Outline each blood parasite and name the species.
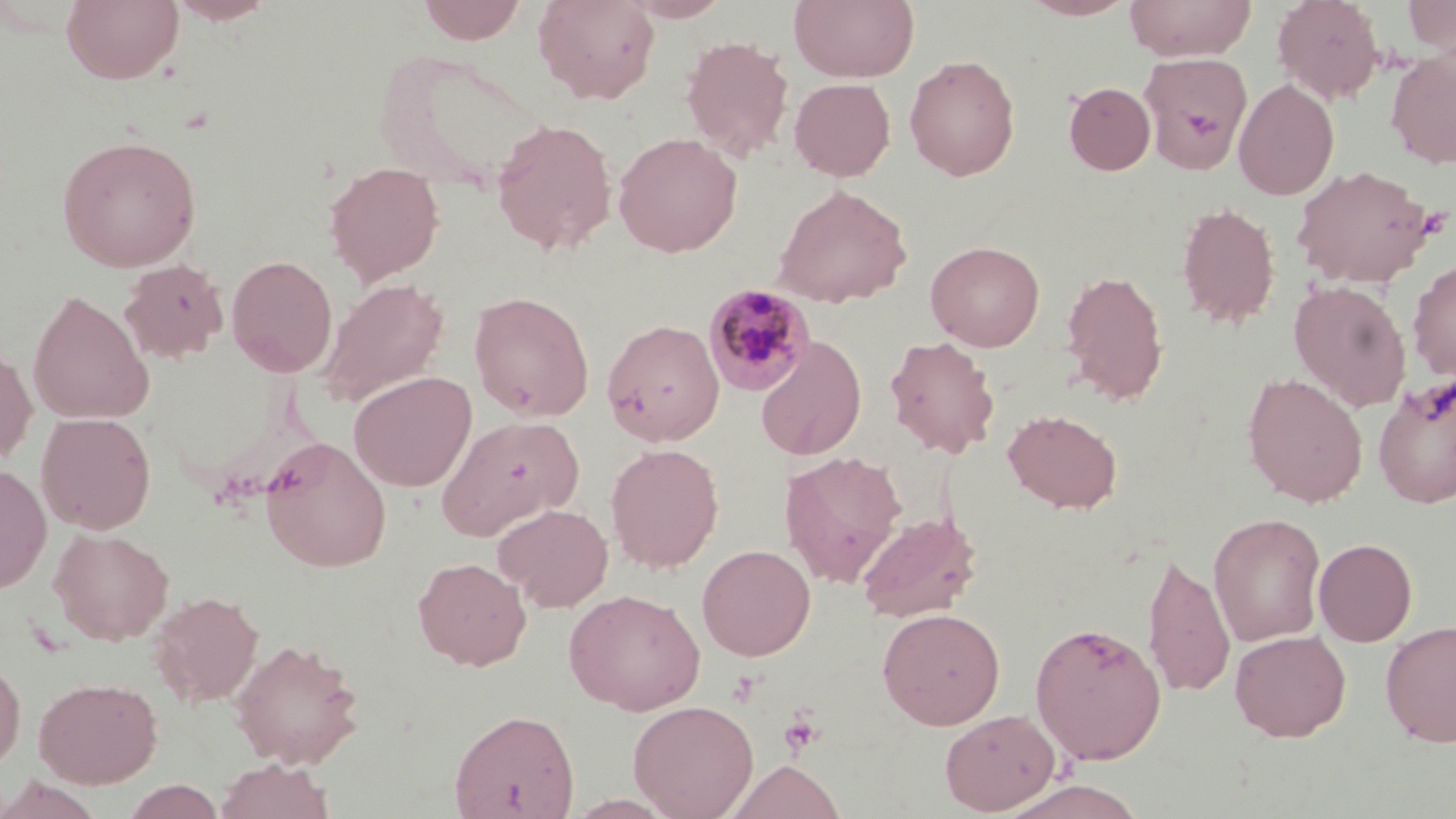

Approximate bounding boxes as [x1, y1, x2, y2] in pixels.
Plasmodium malariae-infected red blood cells: [703, 283, 816, 397].
No Plasmodium falciparum, Plasmodium ovale, Plasmodium vivax, Babesia divergens, or Trypanosoma brucei observed.

Summary:
  - Platelet locations: [777, 709, 825, 759]
  - Uninfected red blood cell locations: [61, 0, 184, 85], [165, 0, 279, 25], [416, 0, 528, 44], [532, 0, 661, 104], [621, 0, 733, 22], [789, 0, 919, 83], [1020, 0, 1138, 20], [1123, 0, 1257, 62], [1272, 0, 1385, 104], [1403, 0, 1455, 58], [680, 35, 794, 162], [375, 50, 551, 196], [1386, 50, 1456, 169], [1138, 52, 1252, 172], [903, 54, 1020, 180], [789, 78, 896, 181], [1233, 79, 1339, 200], [1063, 81, 1155, 175], [491, 118, 618, 255], [613, 132, 743, 257], [56, 135, 202, 272], [324, 161, 444, 285], [1292, 164, 1437, 288], [772, 184, 912, 308], [1176, 202, 1280, 329], [925, 239, 1045, 351], [226, 255, 338, 377], [1407, 258, 1456, 381], [119, 259, 229, 364], [1060, 268, 1169, 404], [319, 278, 449, 407], [1290, 280, 1411, 411], [27, 290, 154, 426], [468, 291, 594, 421], [601, 318, 725, 446], [755, 335, 867, 461], [884, 335, 1000, 459], [0, 342, 38, 468], [348, 370, 477, 491], [1243, 373, 1367, 507], [1372, 374, 1456, 509], [1003, 409, 1122, 513], [36, 412, 156, 534], [437, 414, 585, 540], [259, 436, 393, 572], [605, 443, 724, 572], [779, 450, 907, 587], [0, 464, 52, 593], [493, 502, 613, 612], [857, 511, 982, 623], [1208, 512, 1326, 646], [49, 527, 174, 645], [1314, 538, 1417, 647], [697, 544, 816, 660], [1142, 549, 1236, 698], [412, 556, 531, 670], [564, 588, 705, 715], [149, 591, 264, 708], [877, 607, 1005, 730], [1029, 620, 1167, 764], [1380, 620, 1456, 747], [1230, 629, 1351, 742], [229, 638, 365, 768], [0, 653, 26, 775], [34, 677, 162, 788], [627, 699, 759, 818], [449, 707, 580, 818], [940, 708, 1061, 815], [215, 759, 336, 819], [726, 759, 845, 819], [0, 775, 105, 819], [122, 778, 227, 818], [998, 778, 1149, 819]
  - Slide-level diagnosis: Plasmodium malariae
  - Magnification: 1000x
  - Stain: May-Grünwald-Giemsa
  - Modality: light microscopy
  - Image size: 1456×819 pixels
  - Field of view: one of a larger specimen
  - Preparation: thin blood smear